Outline platelets.
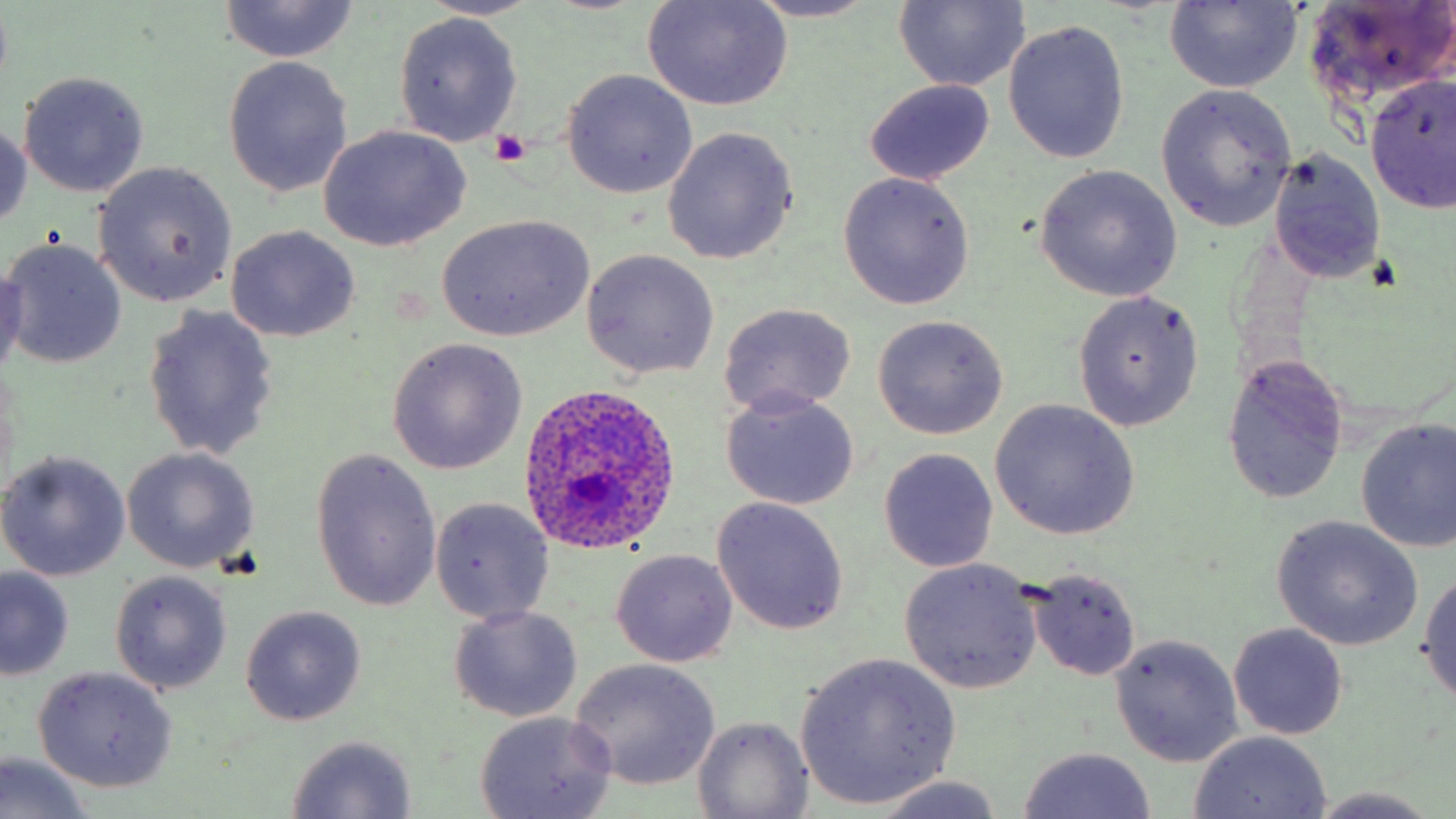
Approximate bounding boxes as (x1, y1, x2, y2) in pixels.
Platelets: (490, 130, 529, 166).

Plasmodium ovale-infected red blood cell locations = approximate bounding boxes as (x1, y1, x2, y2) in pixels: (517, 381, 681, 557)
slide-level diagnosis = Plasmodium ovale
magnification = 1000x
field of view = one of a larger specimen
image size = 1456×819 pixels
uninfected red blood cell locations = approximate bounding boxes as (x1, y1, x2, y2) in pixels: (421, 0, 544, 21), (643, 0, 794, 110), (1303, 0, 1456, 106), (218, 1, 361, 65), (743, 1, 886, 23), (893, 1, 1028, 91), (1164, 1, 1302, 92), (394, 13, 522, 145), (1004, 19, 1128, 162), (221, 56, 352, 197), (560, 69, 698, 198), (17, 71, 150, 196), (1365, 73, 1456, 216), (865, 78, 995, 185), (1156, 83, 1298, 232), (0, 115, 31, 234), (317, 124, 471, 251), (663, 128, 799, 265), (1270, 148, 1386, 287), (93, 162, 238, 308), (1033, 166, 1183, 302), (838, 172, 975, 309), (437, 214, 594, 342), (226, 225, 360, 342), (2, 238, 127, 370), (582, 249, 720, 379), (0, 264, 27, 385), (1072, 291, 1204, 432), (718, 303, 857, 417), (141, 305, 280, 460), (871, 315, 1008, 440), (385, 338, 527, 474), (1221, 354, 1349, 505), (721, 389, 859, 511), (989, 399, 1140, 542), (1354, 416, 1456, 552), (122, 447, 260, 574), (877, 447, 999, 573), (309, 449, 443, 613), (0, 450, 132, 581), (711, 497, 849, 635), (429, 499, 554, 624), (1271, 516, 1425, 651), (611, 549, 738, 668), (900, 559, 1042, 693), (0, 566, 74, 681), (1416, 566, 1456, 706), (1027, 569, 1143, 680), (111, 571, 232, 695), (239, 605, 367, 726), (448, 606, 583, 724), (1228, 623, 1350, 740), (1109, 634, 1244, 767), (795, 652, 961, 809), (569, 658, 721, 791), (32, 665, 178, 793), (473, 710, 617, 819), (694, 715, 812, 818), (1188, 732, 1331, 817), (285, 735, 419, 817), (1016, 746, 1160, 819), (1, 751, 96, 819), (869, 775, 1012, 818), (1302, 788, 1451, 817)
stain = May-Grünwald-Giemsa
preparation = thin blood smear
modality = light microscopy